Classify this cell by malaria status.
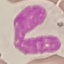
Uninfected.

Giemsa-stained preparation. Thin blood smear. Acquired by smartphone through the microscope eyepiece. Cell patch, automatically extracted from a larger field of view and resized to 64 × 64 pixels.